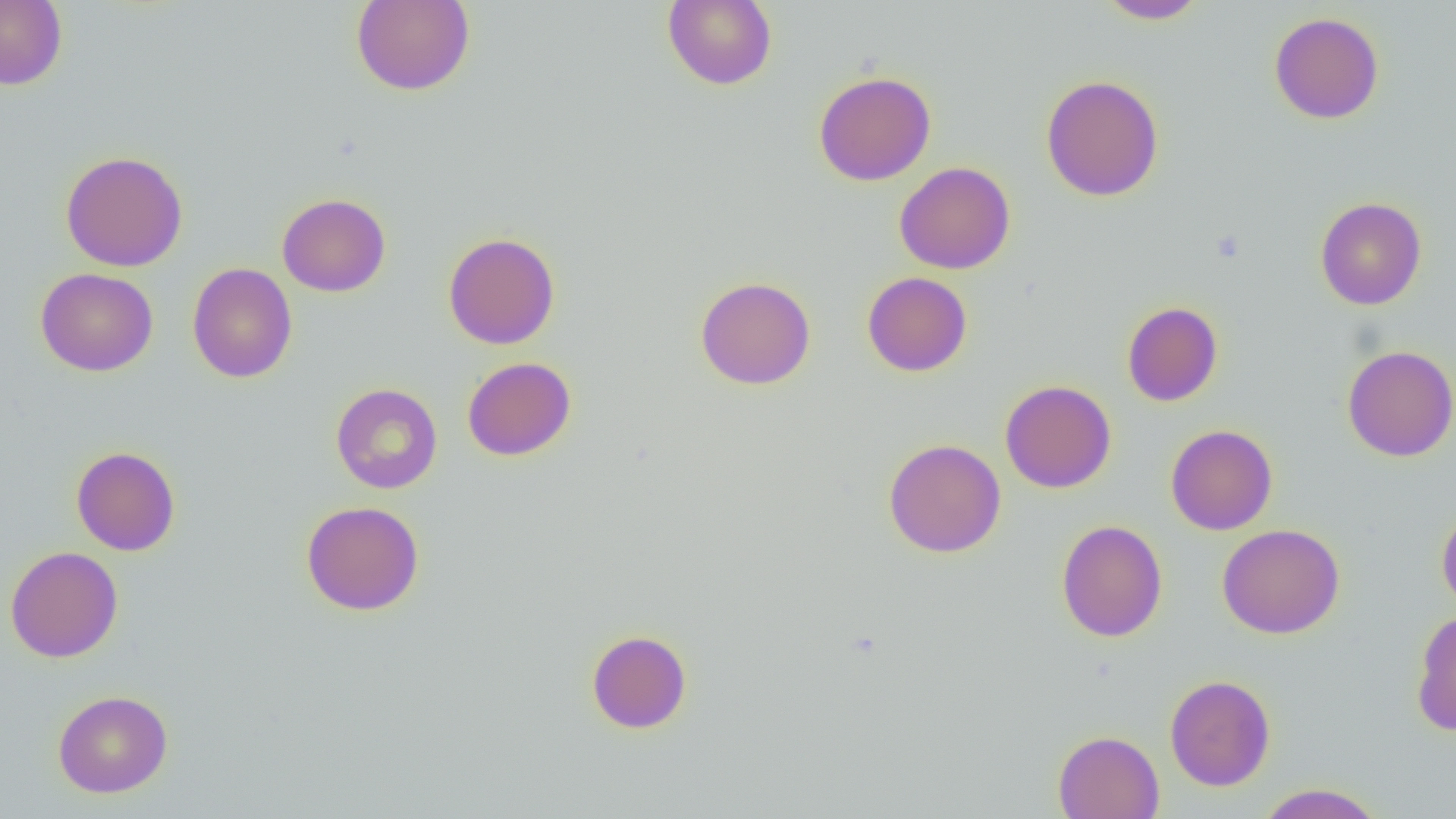
Summary:
  - Coordinate format: approximate bounding boxes as (x1,y1)-(x2,y2) corner pairs in pixels
  - Uninfected red blood cell locations: (0,0)-(67,90), (351,0)-(475,96), (662,0)-(777,90), (1095,0)-(1210,24), (1269,11)-(1384,124), (813,70)-(937,186), (1040,74)-(1164,201), (60,150)-(189,271), (894,161)-(1016,274), (277,193)-(391,297), (1314,196)-(1427,310), (443,231)-(560,350), (187,263)-(298,383), (35,267)-(158,377), (862,272)-(973,377), (695,276)-(816,390), (1121,301)-(1223,406), (1342,345)-(1456,462), (462,357)-(576,461), (1000,379)-(1117,493), (330,383)-(443,493), (1166,424)-(1278,535), (883,439)-(1006,558), (71,446)-(180,556), (301,500)-(425,616), (1436,504)-(1456,615), (1056,519)-(1167,642), (1216,523)-(1345,639), (5,546)-(123,663), (1411,609)-(1456,735), (586,629)-(692,733), (1164,674)-(1276,792), (53,690)-(173,797), (1053,730)-(1164,819), (1254,783)-(1387,819)
  - Slide-level diagnosis: no evidence of blood parasites
  - Preparation: thin blood film
  - Image size: 1456×819 pixels
  - Field of view: single
  - Modality: optical microscopy
  - Magnification: 1000x